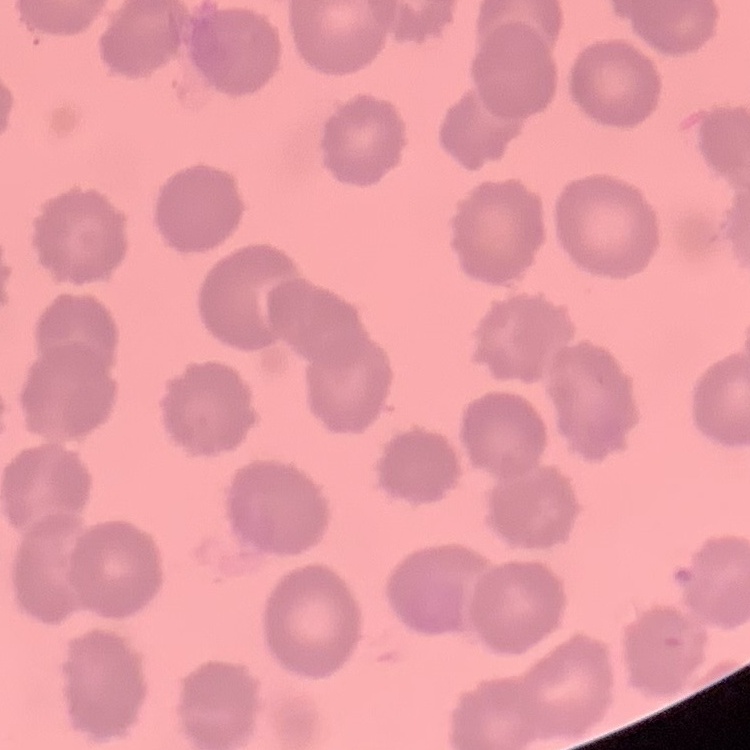
red blood cell morphology = no rouleaux formation
stain = Field's or Giemsa
preparation = thin peripheral smear
image type = square crop of a larger photomicrograph